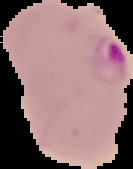
image type = segmented cell region with the area outside set to black
image size = 133×169 pixels
result = malaria parasites detected
preparation = thin blood smear